State the blood parasite species.
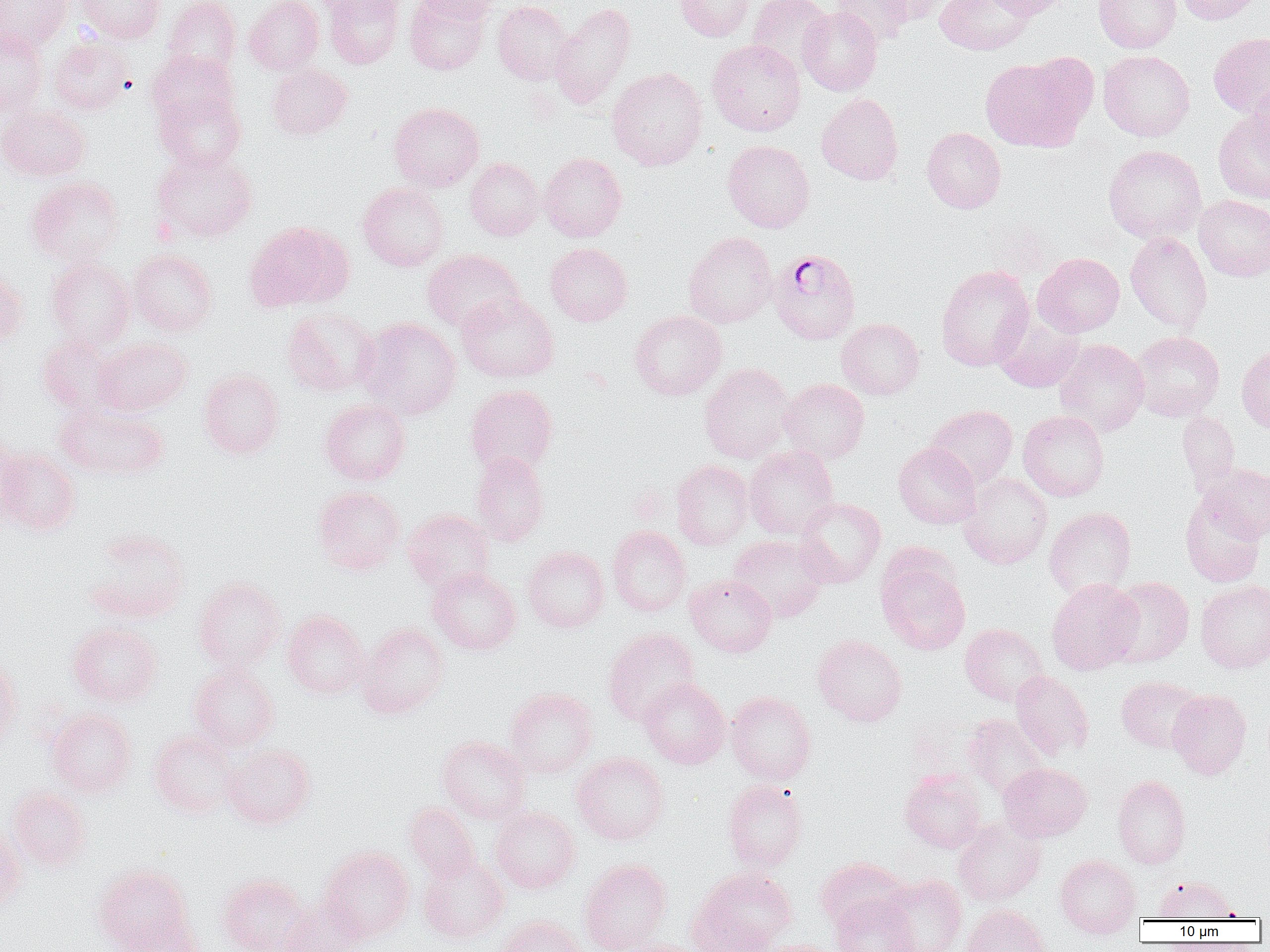

Plasmodium falciparum.

field_of_view: single
uninfected_red_blood_cell_locations: 'approximate bounding boxes as (x1,y1)-(x2,y2) corner pairs in pixels: (0,0)-(72,53), (75,0)-(166,43), (162,0)-(241,81), (244,0)-(324,75), (311,0)-(400,17), (322,0)-(404,69), (405,0)-(490,75), (413,0)-(502,23), (674,0)-(754,41), (748,0)-(833,76), (830,0)-(914,46), (872,0)-(951,25), (935,0)-(1034,55), (986,0)-(1074,20), (1094,0)-(1181,53), (1175,0)-(1263,25), (492,1)-(575,85), (550,3)-(636,110), (798,6)-(883,96), (0,30)-(49,116), (1208,32)-(1270,118), (49,38)-(134,114), (707,39)-(806,136), (147,50)-(238,129), (1098,50)-(1194,141), (979,53)-(1096,152), (267,63)-(352,139), (607,66)-(707,171), (1246,78)-(1270,168), (153,87)-(246,173), (817,93)-(903,185), (388,102)-(485,191), (0,104)-(90,182), (1213,108)-(1270,204), (922,127)-(1006,213), (723,140)-(814,232), (1103,144)-(1206,243), (153,149)-(258,243), (538,152)-(627,242), (465,157)-(543,240), (26,176)-(125,266), (358,182)-(449,271), (1194,195)-(1270,281), (244,220)-(353,313), (683,231)-(777,328), (1125,231)-(1213,334), (545,242)-(632,326), (128,248)-(218,336), (423,249)-(524,333), (1033,253)-(1124,337), (46,257)-(135,349), (936,265)-(1035,371), (0,266)-(28,348), (456,292)-(559,382), (281,307)-(380,396), (630,310)-(726,400), (994,314)-(1084,392), (357,317)-(461,419), (836,318)-(924,400), (1130,331)-(1224,422), (37,333)-(121,415), (93,337)-(193,416), (1054,339)-(1150,436), (1237,345)-(1270,433), (699,362)-(796,464), (198,369)-(284,459), (778,378)-(870,463), (465,384)-(558,477), (319,399)-(410,486), (55,401)-(169,480), (926,405)-(1018,488), (1018,410)-(1109,501), (1178,411)-(1240,491), (0,431)-(29,527), (893,442)-(981,529), (744,445)-(839,539), (1,446)-(81,536), (471,453)-(550,546), (671,460)-(754,550), (1202,463)-(1270,541), (958,473)-(1052,570), (313,485)-(405,575), (1180,493)-(1266,587), (795,497)-(886,588), (1044,506)-(1136,599), (402,509)-(494,594), (608,525)-(691,616), (85,529)-(190,623), (727,534)-(829,622), (522,546)-(610,632), (877,556)-(971,655), (427,567)-(521,655), (685,574)-(777,657), (193,576)-(286,673), (1104,576)-(1194,667), (1046,578)-(1143,675), (1195,579)-(1270,673), (282,610)-(369,699), (67,622)-(162,707), (357,623)-(449,719), (960,623)-(1048,706), (603,627)-(701,726), (812,634)-(907,727), (0,657)-(21,751), (189,664)-(280,751), (1010,670)-(1094,760), (1116,676)-(1204,753), (638,677)-(730,769), (504,687)-(598,777), (1168,689)-(1252,779), (726,691)-(816,784), (46,707)-(137,797), (962,714)-(1049,799), (149,727)-(239,817), (437,735)-(530,824), (222,744)-(316,829), (572,752)-(670,845), (998,762)-(1092,842), (899,769)-(986,853), (1112,774)-(1190,869), (723,779)-(807,871), (6,785)-(91,871), (404,802)-(479,883), (490,807)-(581,893), (952,817)-(1046,906), (0,828)-(26,913), (319,846)-(414,942), (1054,854)-(1141,938), (419,855)-(509,943), (814,856)-(909,931), (579,858)-(673,952), (93,863)-(195,951), (689,867)-(797,952), (217,873)-(310,952), (878,874)-(967,952), (1154,876)-(1235,921), (830,893)-(919,952), (281,898)-(366,952), (961,904)-(1051,952), (119,912)-(205,952), (495,916)-(585,952), (608,939)-(705,952), (757,939)-(844,952)'
magnification: 1000x
image_size: 1270×952 pixels
plasmodium_falciparum_infected_red_blood_cell_locations: 'approximate bounding boxes as (x1,y1)-(x2,y2) corner pairs in pixels: (769,248)-(861,345)'
preparation: thin blood film
modality: optical microscopy